Evaluate for Plasmodium parasites.
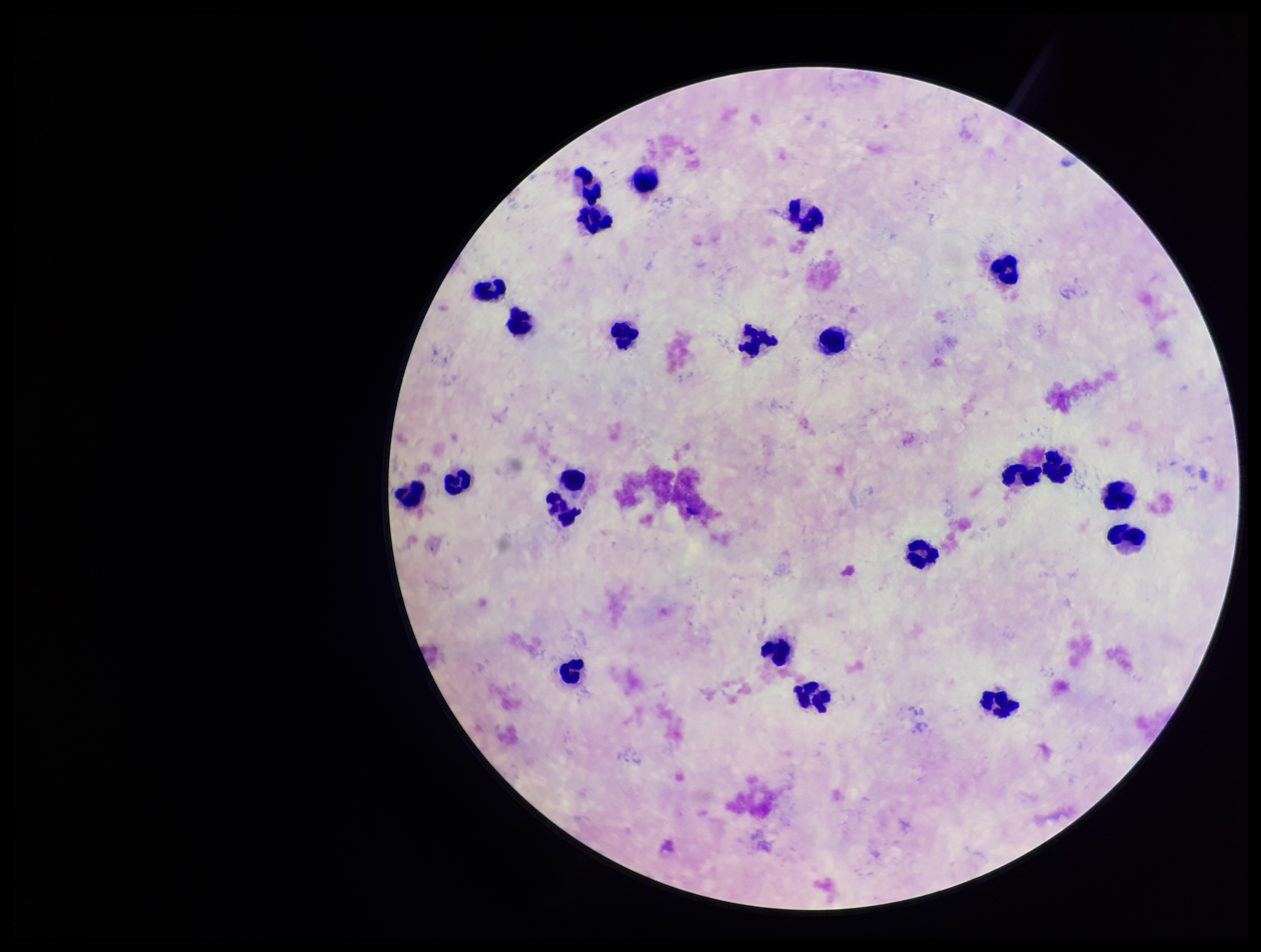

None seen.

capture = smartphone photograph through the microscope eyepiece
leukocyte count = 23
preparation = thick blood smear
stain = Giemsa
image size = 1261×952 pixels
field of view = single
parasite count = 0
patient malaria status = negative